Report the malaria status of this cell.
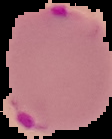
It is parasitized.

From a thin blood film. Image is 112×139 pixels. Segmented cell region on a black background.